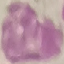
Summary:
  - Result: no malaria parasites detected
  - Capture: smartphone camera at the microscope eyepiece
  - Image type: automatically extracted cell patch, resized to 64 × 64 pixels
  - Preparation: thin blood film
  - Stain: Giemsa